Locate every blood parasite and identify its species.
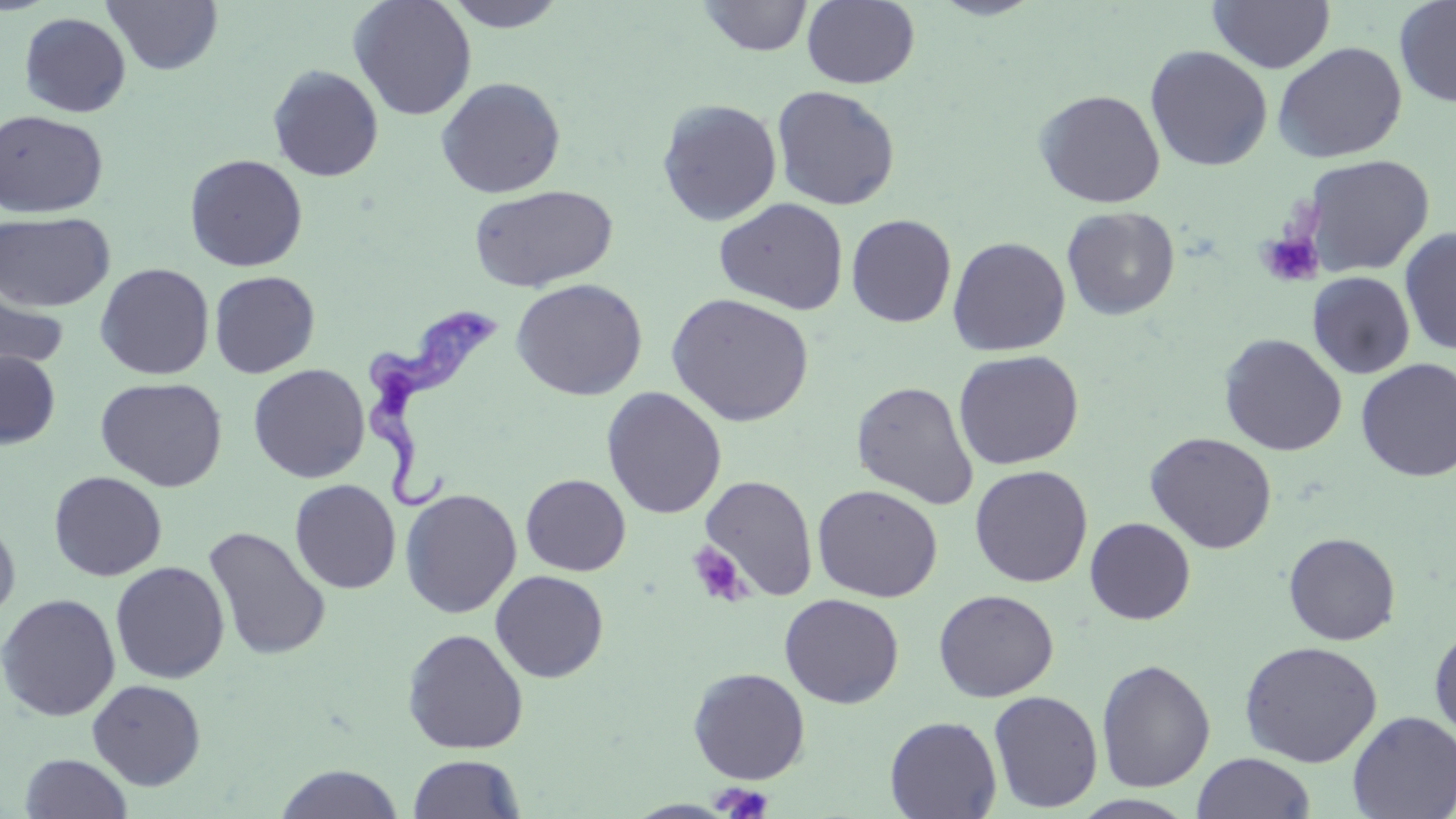

Approximate bounding boxes as named x1/y1/x2/y2 corners in pixels.
Trypanosoma brucei: (x1=354, y1=306, x2=508, y2=515).
No Plasmodium falciparum, Plasmodium ovale, Plasmodium malariae, Plasmodium vivax, or Babesia divergens observed.

Summary:
  - Uninfected red blood cell locations: (x1=103, y1=0, x2=224, y2=75), (x1=348, y1=0, x2=477, y2=121), (x1=441, y1=0, x2=571, y2=32), (x1=698, y1=0, x2=813, y2=56), (x1=928, y1=0, x2=1046, y2=21), (x1=1394, y1=0, x2=1456, y2=108), (x1=801, y1=1, x2=920, y2=89), (x1=1208, y1=1, x2=1335, y2=73), (x1=19, y1=11, x2=131, y2=118), (x1=1272, y1=41, x2=1408, y2=163), (x1=1144, y1=45, x2=1273, y2=172), (x1=267, y1=64, x2=384, y2=181), (x1=436, y1=76, x2=566, y2=198), (x1=771, y1=85, x2=901, y2=211), (x1=1033, y1=89, x2=1165, y2=208), (x1=657, y1=98, x2=782, y2=226), (x1=0, y1=109, x2=109, y2=218), (x1=184, y1=153, x2=308, y2=272), (x1=1303, y1=154, x2=1435, y2=276), (x1=468, y1=184, x2=618, y2=293), (x1=714, y1=197, x2=849, y2=316), (x1=1062, y1=206, x2=1181, y2=321), (x1=0, y1=211, x2=115, y2=312), (x1=846, y1=214, x2=957, y2=328), (x1=1399, y1=226, x2=1456, y2=356), (x1=947, y1=236, x2=1070, y2=356), (x1=94, y1=263, x2=215, y2=380), (x1=208, y1=270, x2=320, y2=379), (x1=1308, y1=272, x2=1415, y2=379), (x1=0, y1=275, x2=69, y2=385), (x1=510, y1=278, x2=648, y2=401), (x1=665, y1=292, x2=815, y2=427), (x1=1218, y1=333, x2=1347, y2=456), (x1=0, y1=350, x2=60, y2=450), (x1=953, y1=350, x2=1084, y2=470), (x1=1355, y1=358, x2=1456, y2=482), (x1=248, y1=363, x2=370, y2=484), (x1=95, y1=376, x2=228, y2=492), (x1=850, y1=380, x2=979, y2=509), (x1=601, y1=386, x2=727, y2=520), (x1=1144, y1=431, x2=1277, y2=553), (x1=969, y1=464, x2=1093, y2=588), (x1=48, y1=471, x2=167, y2=581), (x1=520, y1=473, x2=631, y2=576), (x1=699, y1=475, x2=818, y2=601), (x1=289, y1=479, x2=401, y2=594), (x1=812, y1=484, x2=943, y2=602), (x1=400, y1=488, x2=522, y2=618), (x1=0, y1=514, x2=21, y2=629), (x1=1084, y1=517, x2=1196, y2=624), (x1=203, y1=525, x2=331, y2=661), (x1=1282, y1=532, x2=1401, y2=645), (x1=110, y1=561, x2=230, y2=684), (x1=490, y1=570, x2=609, y2=682), (x1=933, y1=589, x2=1059, y2=702), (x1=0, y1=593, x2=120, y2=722), (x1=779, y1=593, x2=904, y2=709), (x1=1428, y1=622, x2=1456, y2=746), (x1=402, y1=628, x2=529, y2=754), (x1=1239, y1=640, x2=1383, y2=768), (x1=1096, y1=658, x2=1215, y2=792), (x1=688, y1=666, x2=811, y2=785), (x1=87, y1=678, x2=206, y2=790), (x1=988, y1=690, x2=1104, y2=813), (x1=1347, y1=710, x2=1456, y2=819), (x1=884, y1=715, x2=1002, y2=819), (x1=18, y1=752, x2=133, y2=818), (x1=1192, y1=752, x2=1316, y2=819), (x1=407, y1=754, x2=525, y2=818), (x1=274, y1=764, x2=405, y2=819)
  - Platelet locations: (x1=1256, y1=230, x2=1324, y2=288), (x1=687, y1=541, x2=750, y2=607), (x1=716, y1=783, x2=772, y2=819)
  - Slide-level diagnosis: Trypanosoma brucei
  - Image size: 1456×819 pixels
  - Preparation: thin blood film
  - Magnification: 1000x
  - Stain: May-Grünwald-Giemsa
  - Modality: optical microscopy
  - Field of view: one of a larger specimen